Give the position of every Plasmodium parasite visible.
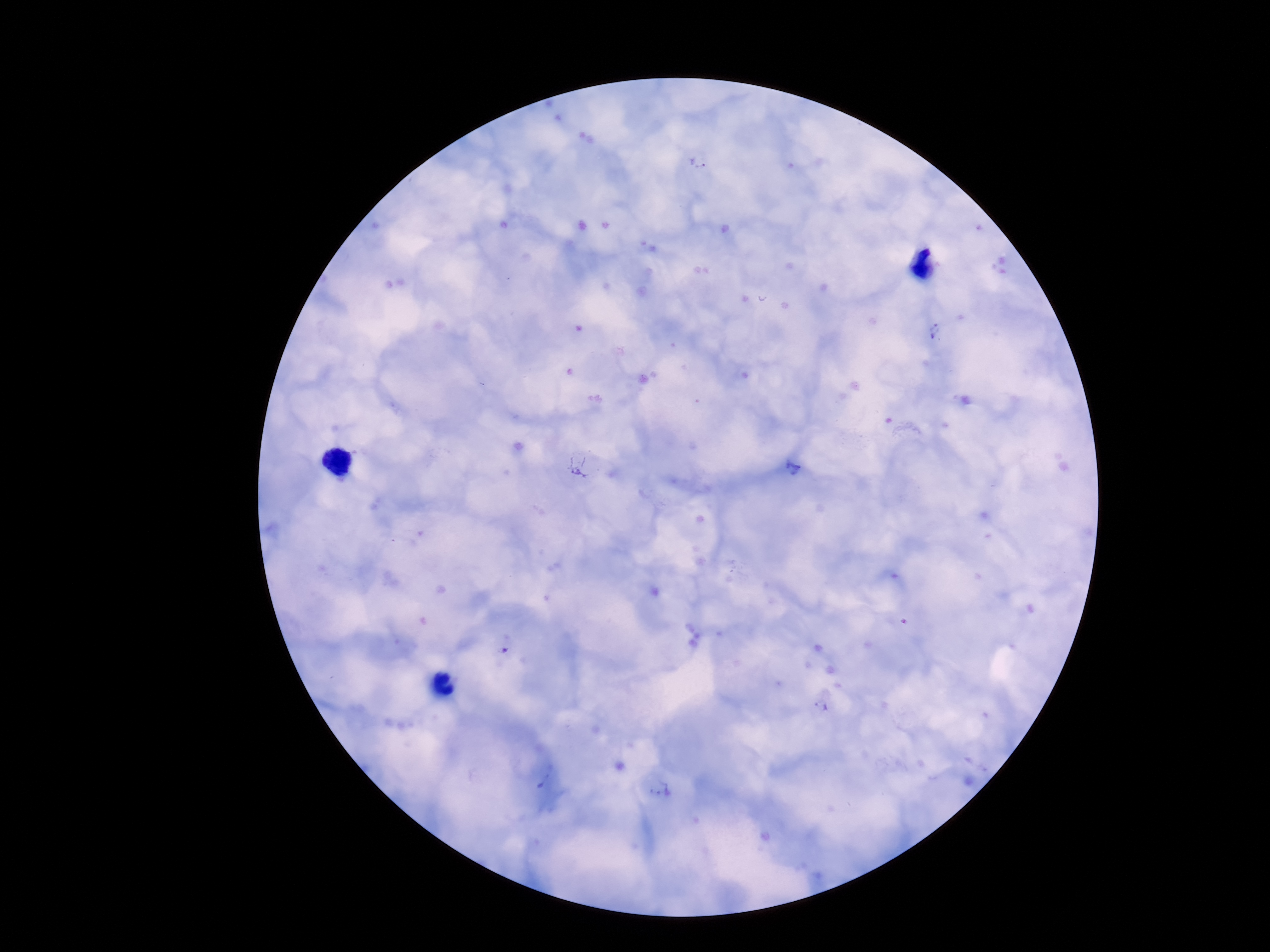
Approximate object centers, in pixels from the top-left corner.
Plasmodium parasites: (x=699, y=162), (x=935, y=331), (x=579, y=466), (x=792, y=467), (x=822, y=705), (x=544, y=779), (x=660, y=789).

100x magnification. Thick blood film. Patient malaria status: infected. Image is 1270×952 pixels. Single field of view. Smartphone photograph taken through the microscope eyepiece. Giemsa stain.